Locate and identify every blood parasite.
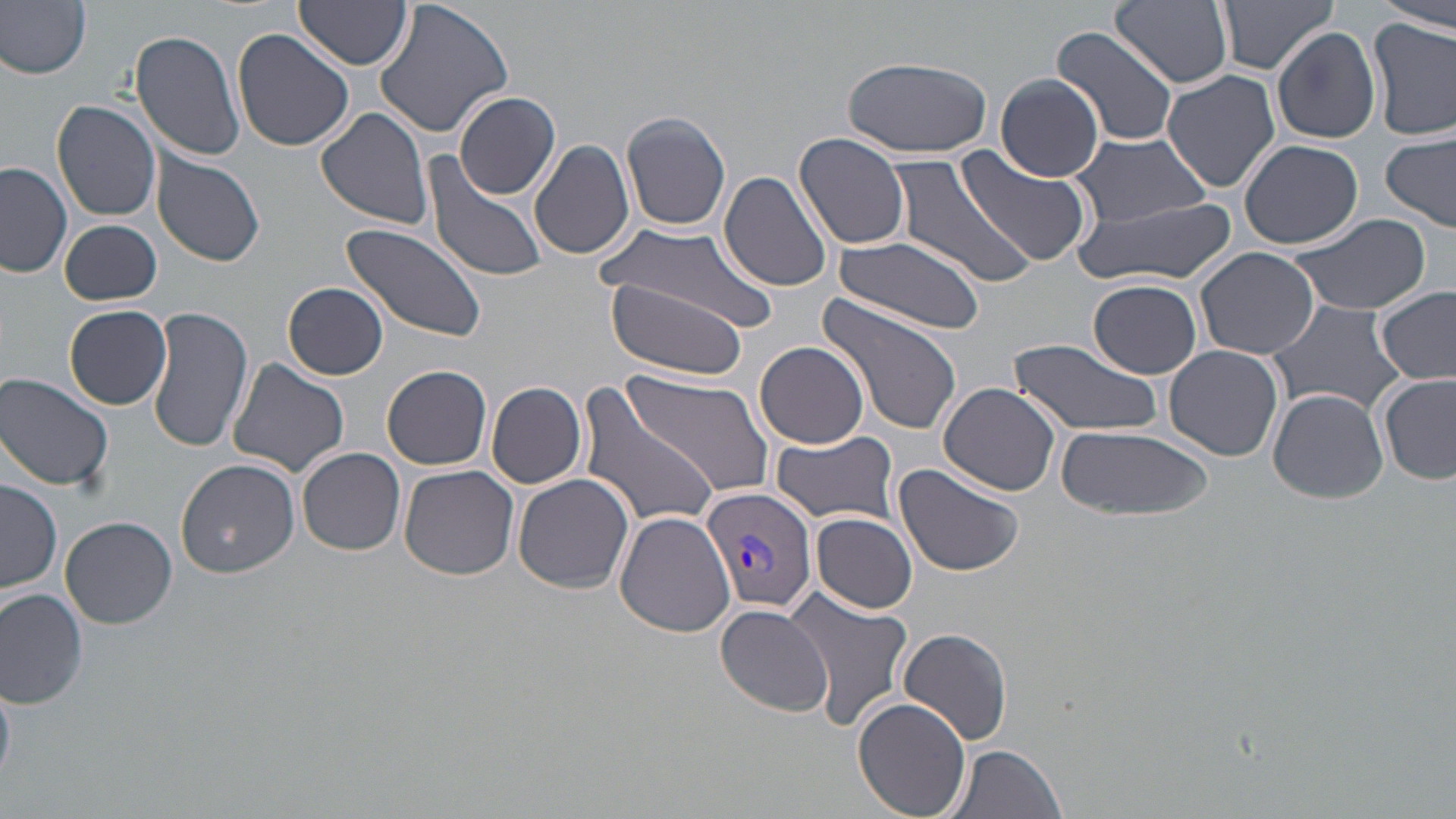

Approximate bounding boxes as named x1/y1/x2/y2 corners in pixels.
Plasmodium vivax-infected red blood cells: (x1=701, y1=487, x2=818, y2=616).
No Plasmodium falciparum, Plasmodium ovale, Plasmodium malariae, Babesia divergens, or Trypanosoma brucei observed.

Uninfected red blood cell locations: (x1=0, y1=0, x2=93, y2=81), (x1=374, y1=0, x2=516, y2=140), (x1=1111, y1=0, x2=1232, y2=89), (x1=1375, y1=0, x2=1456, y2=32), (x1=1215, y1=1, x2=1340, y2=79), (x1=294, y1=2, x2=412, y2=71), (x1=1368, y1=17, x2=1456, y2=141), (x1=1053, y1=26, x2=1179, y2=148), (x1=130, y1=27, x2=249, y2=161), (x1=1272, y1=27, x2=1380, y2=145), (x1=233, y1=28, x2=357, y2=152), (x1=842, y1=55, x2=994, y2=159), (x1=1162, y1=69, x2=1280, y2=194), (x1=996, y1=74, x2=1106, y2=179), (x1=453, y1=92, x2=561, y2=200), (x1=52, y1=100, x2=162, y2=221), (x1=314, y1=105, x2=437, y2=231), (x1=621, y1=111, x2=731, y2=232), (x1=1070, y1=131, x2=1211, y2=226), (x1=1381, y1=132, x2=1456, y2=231), (x1=794, y1=134, x2=912, y2=250), (x1=1239, y1=138, x2=1363, y2=249), (x1=529, y1=139, x2=636, y2=260), (x1=152, y1=152, x2=266, y2=269), (x1=887, y1=152, x2=1038, y2=290), (x1=419, y1=153, x2=550, y2=284), (x1=960, y1=153, x2=1096, y2=272), (x1=0, y1=160, x2=74, y2=279), (x1=720, y1=170, x2=833, y2=292), (x1=1075, y1=196, x2=1237, y2=288), (x1=1288, y1=213, x2=1433, y2=315), (x1=60, y1=218, x2=162, y2=306), (x1=339, y1=223, x2=484, y2=343), (x1=599, y1=227, x2=772, y2=326), (x1=831, y1=236, x2=987, y2=335), (x1=1195, y1=247, x2=1320, y2=359), (x1=602, y1=277, x2=756, y2=380), (x1=1089, y1=279, x2=1202, y2=379), (x1=283, y1=282, x2=389, y2=380), (x1=1375, y1=287, x2=1455, y2=386), (x1=816, y1=294, x2=965, y2=437), (x1=1264, y1=298, x2=1411, y2=420), (x1=64, y1=305, x2=172, y2=410), (x1=147, y1=305, x2=250, y2=454), (x1=1008, y1=336, x2=1164, y2=438), (x1=755, y1=341, x2=870, y2=449), (x1=1163, y1=345, x2=1284, y2=461), (x1=223, y1=358, x2=351, y2=479), (x1=620, y1=364, x2=774, y2=505), (x1=383, y1=366, x2=493, y2=470), (x1=0, y1=372, x2=116, y2=494), (x1=1378, y1=372, x2=1456, y2=486), (x1=574, y1=380, x2=722, y2=532), (x1=486, y1=382, x2=588, y2=488), (x1=938, y1=383, x2=1063, y2=494), (x1=1268, y1=389, x2=1388, y2=502), (x1=1058, y1=424, x2=1215, y2=523), (x1=771, y1=432, x2=899, y2=523), (x1=298, y1=448, x2=406, y2=556), (x1=175, y1=458, x2=299, y2=577), (x1=892, y1=463, x2=1025, y2=576), (x1=400, y1=465, x2=520, y2=580), (x1=513, y1=471, x2=636, y2=594), (x1=1, y1=478, x2=62, y2=595), (x1=614, y1=510, x2=736, y2=638), (x1=813, y1=512, x2=918, y2=613), (x1=60, y1=516, x2=178, y2=629), (x1=784, y1=587, x2=913, y2=731), (x1=0, y1=590, x2=88, y2=711), (x1=713, y1=603, x2=833, y2=716), (x1=897, y1=628, x2=1012, y2=748), (x1=853, y1=697, x2=972, y2=819), (x1=944, y1=743, x2=1069, y2=819). Slide-level diagnosis: Plasmodium vivax. Image is 1456×819 pixels. May-Grünwald-Giemsa stain. Captured at 1000x magnification. Single field of view. Light microscopy. Thin blood film.